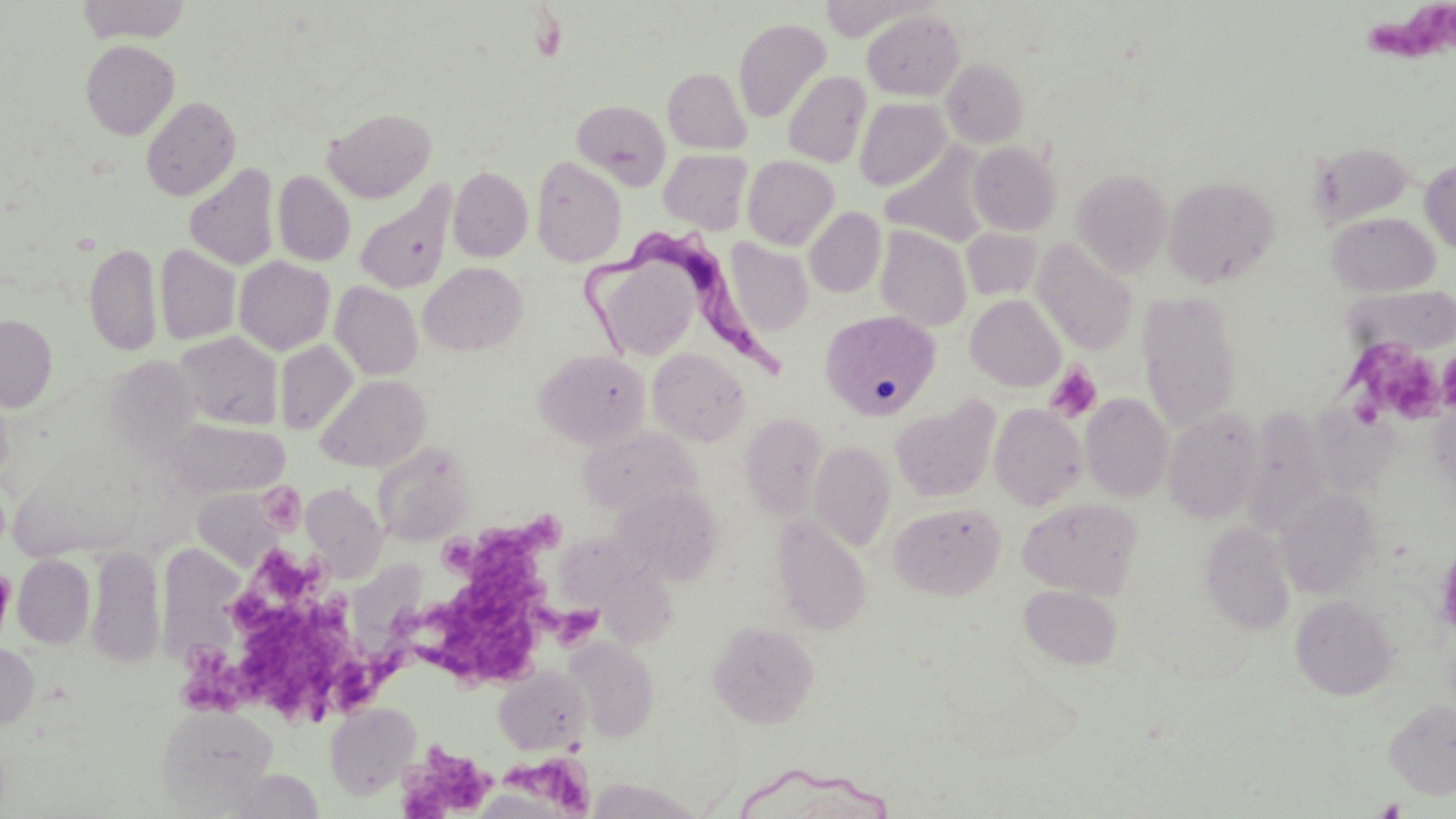

slide-level diagnosis = Trypanosoma brucei
uninfected red blood cell locations = approximate bounding boxes as [x1, y1, x2, y2] in pixels: [818, 0, 928, 42], [76, 1, 191, 43], [862, 9, 965, 100], [733, 18, 831, 123], [81, 39, 179, 140], [941, 58, 1030, 148], [663, 67, 751, 153], [783, 70, 871, 168], [141, 95, 241, 201], [854, 98, 951, 190], [572, 99, 671, 189], [323, 106, 437, 203], [1311, 141, 1413, 227], [967, 142, 1062, 235], [881, 144, 993, 247], [658, 148, 753, 233], [742, 155, 839, 249], [531, 156, 627, 267], [1420, 159, 1456, 255], [184, 162, 279, 270], [448, 166, 533, 262], [1072, 168, 1173, 276], [273, 170, 355, 266], [1163, 175, 1281, 287], [354, 182, 457, 296], [804, 207, 886, 297], [1327, 212, 1441, 297], [875, 226, 973, 331], [962, 227, 1042, 301], [726, 237, 814, 336], [1032, 239, 1138, 355], [84, 241, 162, 356], [155, 245, 241, 345], [234, 256, 334, 355], [607, 262, 702, 355], [418, 263, 529, 356], [330, 281, 423, 379], [1345, 285, 1456, 356], [1137, 290, 1243, 431], [965, 294, 1066, 392], [819, 310, 942, 421], [1, 314, 57, 412], [173, 331, 283, 430], [274, 341, 357, 435], [648, 348, 751, 446], [534, 349, 652, 448], [109, 354, 201, 469], [317, 374, 430, 472], [1081, 393, 1173, 502], [891, 396, 1000, 503], [1429, 401, 1456, 496], [989, 404, 1088, 510], [1164, 408, 1264, 523], [1243, 409, 1330, 536], [739, 412, 829, 518], [165, 418, 288, 499], [578, 427, 700, 518], [809, 440, 896, 551], [374, 445, 472, 545], [301, 484, 387, 580], [613, 485, 726, 585], [192, 487, 289, 569], [1276, 489, 1381, 598], [1017, 497, 1144, 599], [889, 501, 1007, 601], [773, 515, 872, 635], [1201, 521, 1295, 634], [562, 531, 680, 650], [164, 541, 241, 663], [87, 545, 165, 667], [12, 554, 95, 648], [1019, 584, 1123, 670], [1291, 595, 1397, 700], [707, 620, 820, 729], [567, 639, 659, 740], [0, 642, 39, 733], [493, 667, 591, 755], [1385, 700, 1456, 798], [325, 701, 420, 799], [156, 705, 278, 810], [588, 778, 704, 819]
field of view = one of a larger specimen
stain = May-Grünwald-Giemsa
image size = 1456×819 pixels
platelet locations = approximate bounding boxes as [x1, y1, x2, y2] in pixels: [1361, 7, 1455, 70], [1361, 341, 1446, 426], [1437, 348, 1456, 414], [1045, 363, 1102, 422], [421, 521, 583, 680], [185, 561, 402, 722], [398, 742, 497, 819], [509, 757, 595, 816]
magnification = 1000x
modality = light microscopy
preparation = thin blood smear
Trypanosoma brucei locations = approximate bounding boxes as [x1, y1, x2, y2] in pixels: [572, 226, 783, 387]